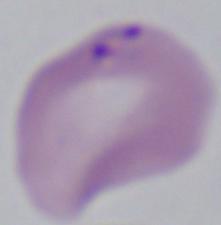

A Babesia parasite is seen. 1000x magnification. Micrograph.